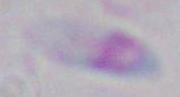

magnification = 1000x
modality = micrograph
identification = Toxoplasma gondii